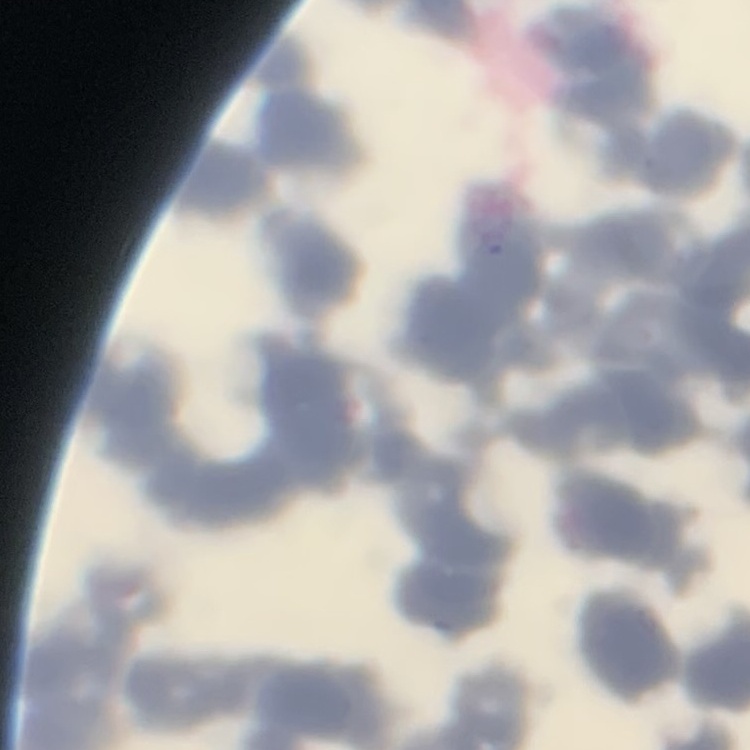
Summary:
  - Red blood cell morphology: rouleaux formation
  - Preparation: thin blood film
  - Stain: Field's or Giemsa
  - Image type: square crop of a larger photomicrograph